Comment on the morphology of the red blood cells.
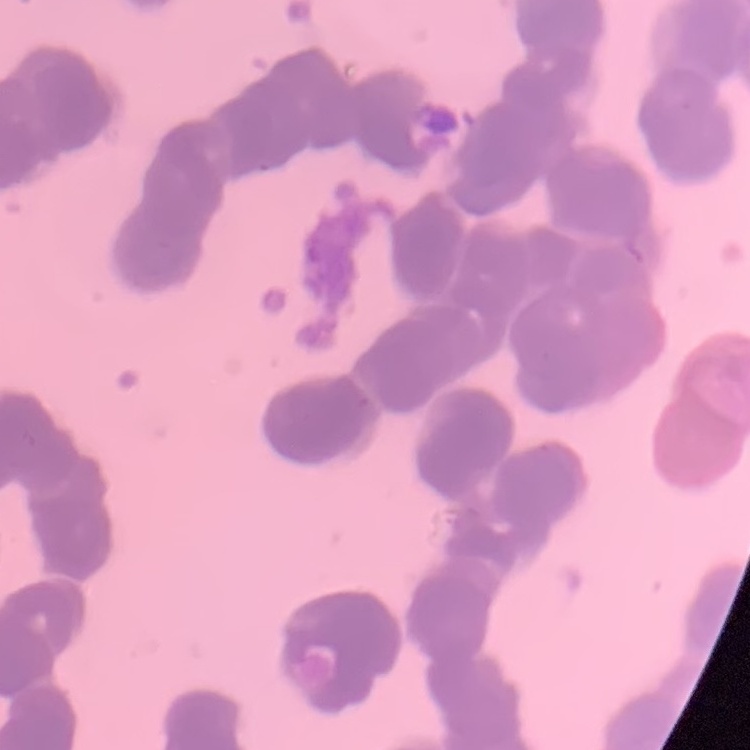

Rouleaux formation.

stain = Field's or Giemsa
preparation = thin peripheral smear
image type = one tile cut from a larger photomicrograph